Classify this cell by malaria status.
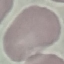
Uninfected.

Summary:
  - Stain: Giemsa
  - Image type: cell patch, automatically extracted from a larger field of view and resized to 64 × 64 pixels
  - Capture: smartphone camera at the microscope eyepiece
  - Preparation: thin blood film